Assess this cell for malaria.
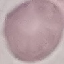

Uninfected.

Giemsa stain. Photographed with a smartphone camera at the microscope eyepiece. Cell patch, automatically extracted from a larger field of view and resized to 64 × 64 pixels. Thin blood smear.